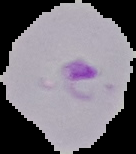
Summary:
  - Preparation: thin blood smear
  - Malaria status: parasitized
  - Image size: 136×154 pixels
  - Image type: cell region segmented out of the field of view; surrounding area masked to black